Report the malaria status of this cell.
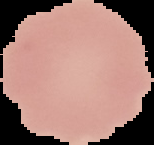

Uninfected.

Summary:
  - Preparation: thin blood film
  - Image size: 154×145 pixels
  - Image type: cell region segmented out of the field of view; surrounding area masked to black